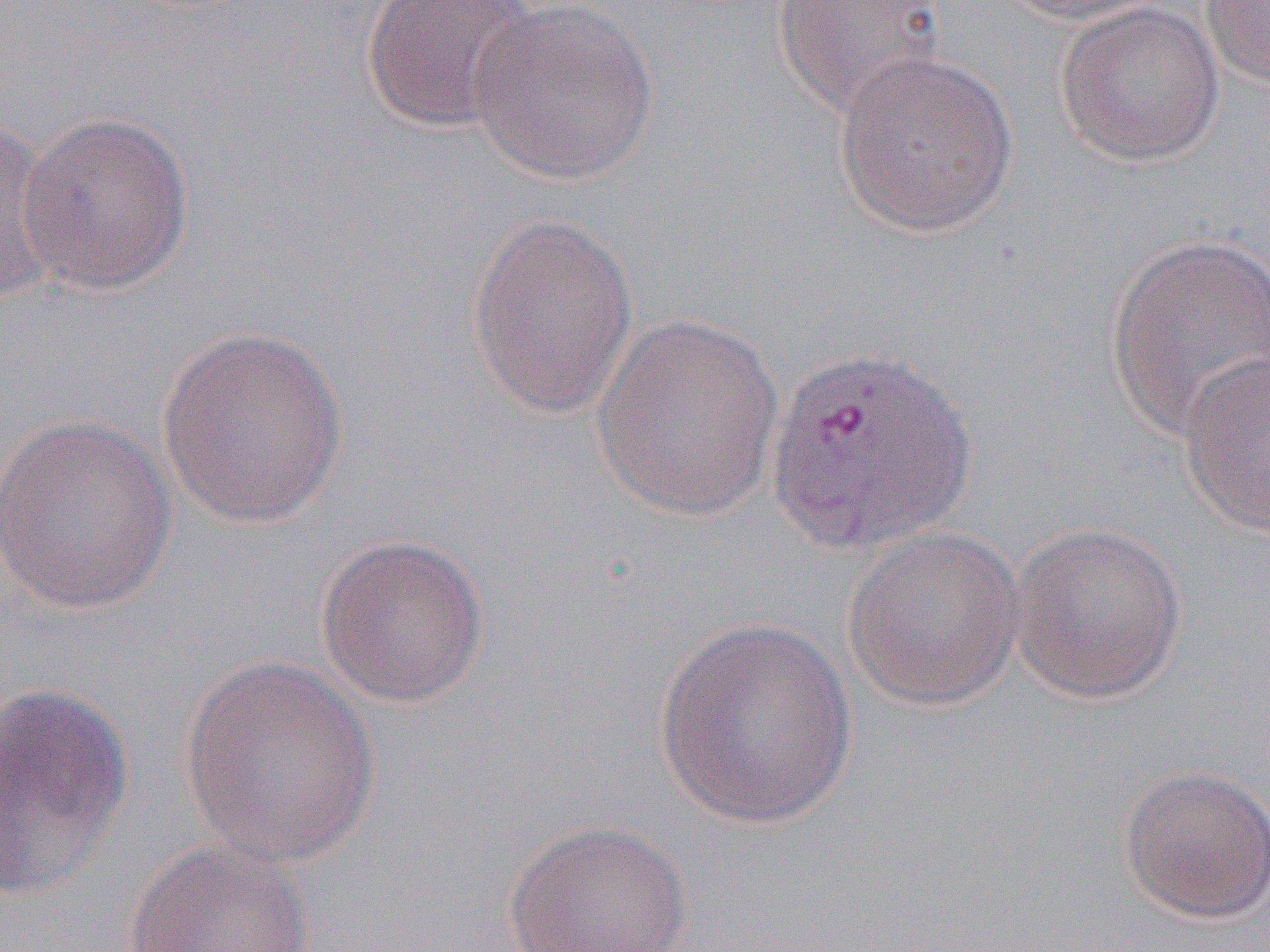

Summary:
  - Coordinate format: approximate bounding boxes as named x1/y1/x2/y2 corners in pixels
  - Uninfected red blood cell locations: (x1=361, y1=0, x2=541, y2=137), (x1=1000, y1=0, x2=1175, y2=28), (x1=1199, y1=0, x2=1270, y2=90), (x1=772, y1=1, x2=948, y2=118), (x1=466, y1=2, x2=659, y2=186), (x1=1053, y1=2, x2=1224, y2=168), (x1=832, y1=48, x2=1019, y2=238), (x1=15, y1=111, x2=195, y2=296), (x1=0, y1=115, x2=61, y2=304), (x1=466, y1=212, x2=640, y2=420), (x1=1105, y1=234, x2=1270, y2=441), (x1=590, y1=310, x2=785, y2=523), (x1=156, y1=325, x2=350, y2=529), (x1=1178, y1=348, x2=1270, y2=539), (x1=1, y1=411, x2=179, y2=617), (x1=1008, y1=520, x2=1188, y2=705), (x1=842, y1=524, x2=1028, y2=712), (x1=313, y1=532, x2=490, y2=709), (x1=652, y1=616, x2=860, y2=828), (x1=179, y1=657, x2=381, y2=867), (x1=0, y1=681, x2=136, y2=902), (x1=1117, y1=764, x2=1270, y2=925), (x1=501, y1=819, x2=694, y2=952), (x1=123, y1=837, x2=318, y2=951)
  - Slide-level diagnosis: Plasmodium vivax
  - Preparation: thin blood smear
  - Modality: light microscopy
  - Image size: 1270×952 pixels
  - Field of view: single
  - Magnification: 1000x